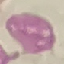

result: no malaria parasites detected
stain: Giemsa
capture: smartphone camera at the microscope eyepiece
image_type: automatically extracted cell patch, resized to 64 × 64 pixels
preparation: thin blood smear